Look for Plasmodium parasites.
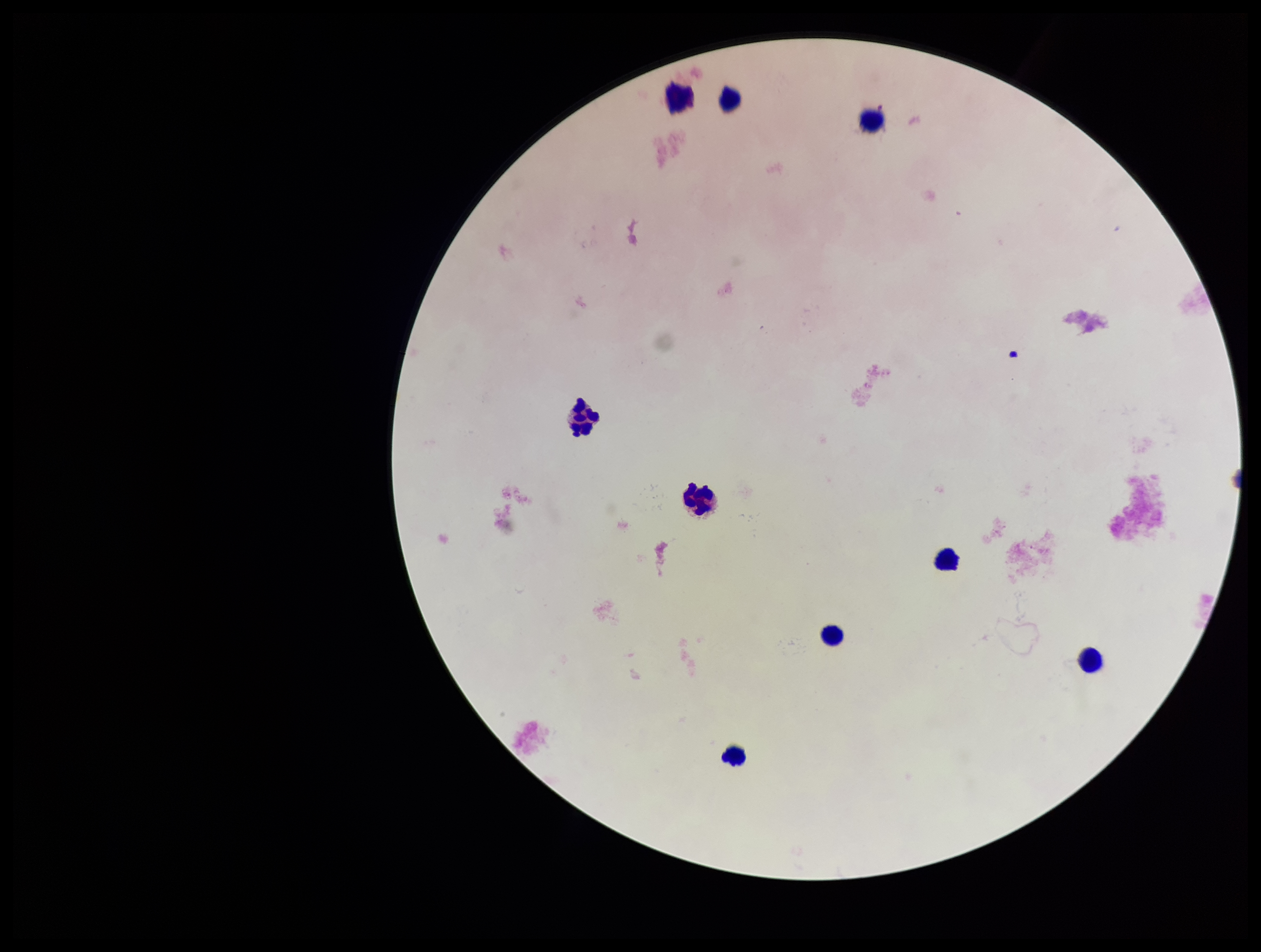

None identified.

field_of_view: one from this slide
patient_malaria_status: negative
leukocyte_count: 9
parasite_count: 0
capture: smartphone photograph through the microscope eyepiece
preparation: thick blood smear
image_size: 1261×952 pixels
stain: Giemsa